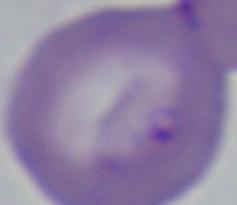

Summary:
  - Magnification: 1000x
  - Identification: Babesia
  - Modality: micrograph